Report the malaria status of this cell.
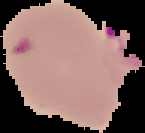

It is parasitized.

{
  "preparation": "thin blood smear",
  "image_type": "segmented cell region on a black background",
  "image_size": "145×133 pixels"
}